Assess this cell for malaria.
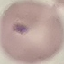

Parasitized.

Acquired by smartphone through the microscope eyepiece. Giemsa-stained preparation. Thin smear of blood. Cell patch, automatically extracted from a larger field of view and resized to 64 × 64 pixels.